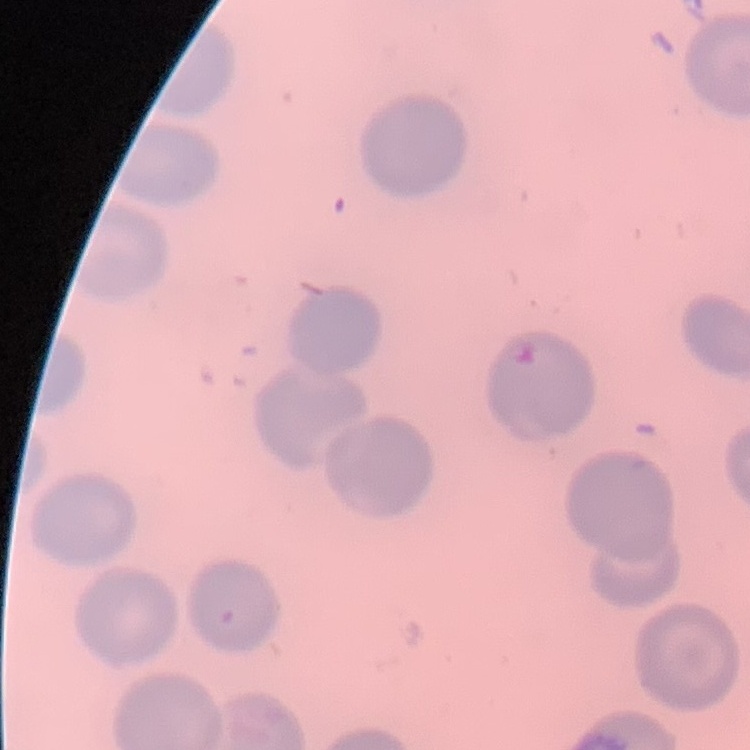
The red blood cells show no rouleaux formation. Stained with either Field's or Giemsa. Thin blood film. Square crop of a larger photomicrograph.